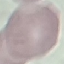
malaria status = uninfected
image type = automatically extracted cell patch, resized to 64 × 64 pixels
capture = smartphone through the microscope eyepiece
stain = Giemsa
preparation = thin blood smear